Assess the morphology of the erythrocytes.
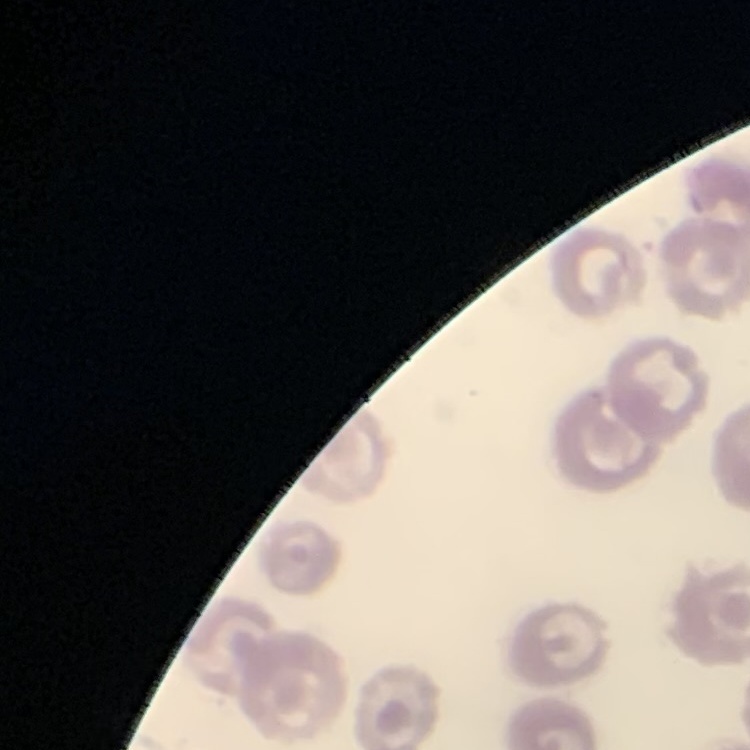
They show no rouleaux formation.

Square crop of a larger photomicrograph. Thin peripheral smear. Stained with either Field's or Giemsa.